Locate Plasmodium parasites and leukocytes.
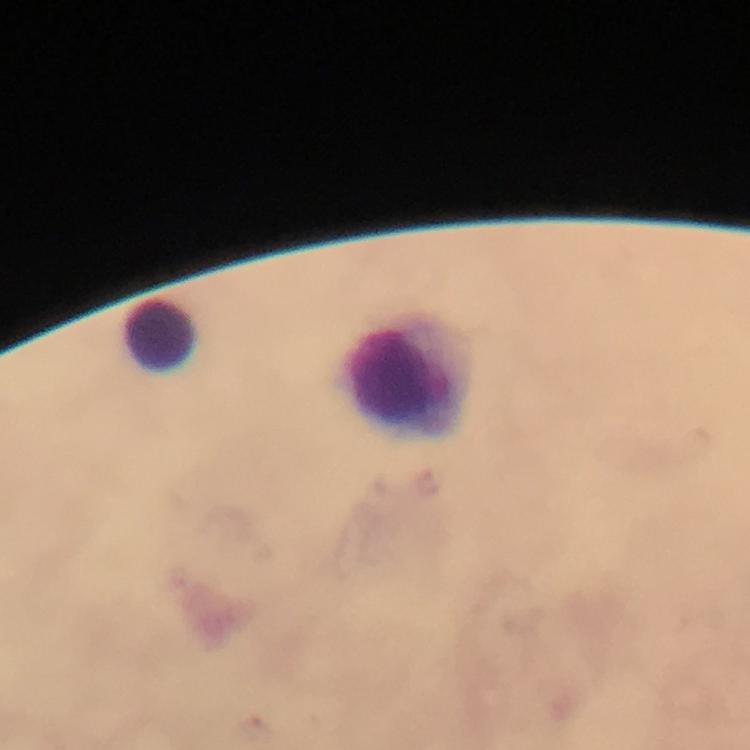

No Plasmodium parasites detected.
Approximate centers as [x, y] in pixels.
Leukocytes: [161, 333], [412, 378].

Summary:
  - Stain: Giemsa
  - Cropped from: one field of view
  - Context: from a malaria diagnostic workup
  - Magnification: 100x
  - Preparation: thick blood smear
  - Immersion oil: used
  - Capture: smartphone camera through the microscope
  - Image size: 750×750 pixels